Comment on the morphology of the red blood cells.
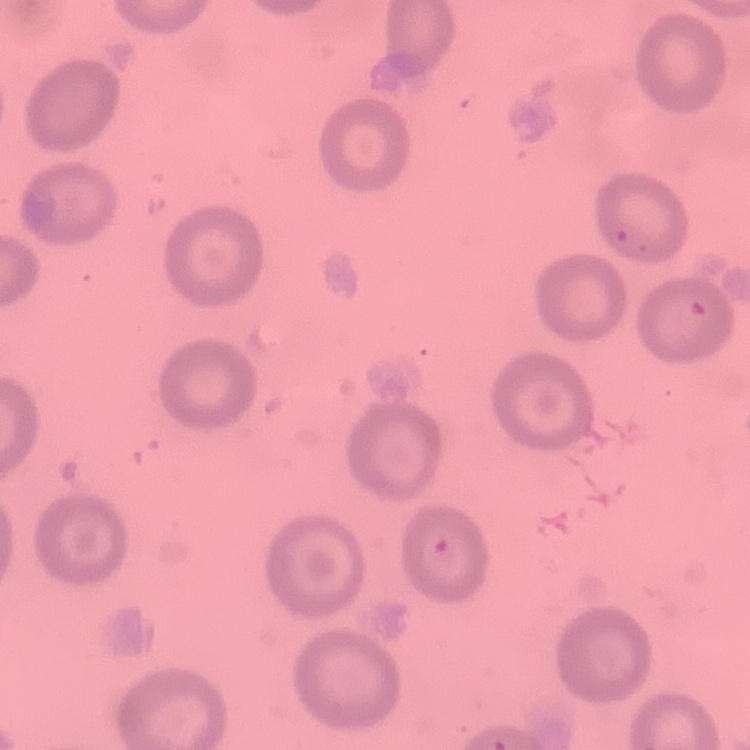

No rouleaux formation.

{
  "preparation": "thin blood film",
  "stain": "Field's or Giemsa",
  "image_type": "one tile cut from a larger photomicrograph"
}